Report the malaria status of this cell.
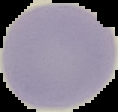

It is uninfected.

preparation = thin blood smear
image size = 118×112 pixels
image type = segmented cell region on a black background